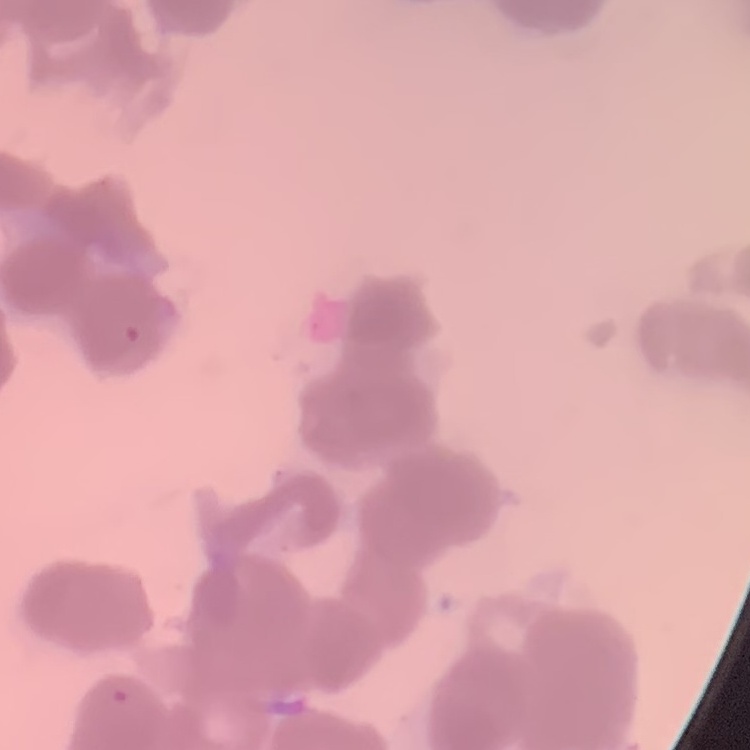
red blood cell morphology = rouleaux formation
image type = square crop of a larger photomicrograph
stain = Field's or Giemsa
preparation = thin peripheral smear